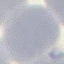

Malaria status: uninfected. Thin blood smear. Giemsa stain. Photographed with a smartphone camera at the microscope eyepiece. Cell patch, automatically extracted from a larger field of view and resized to 64 × 64 pixels.